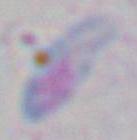

Summary:
  - Modality: photomicrograph
  - Magnification: 1000x
  - Identification: Toxoplasma gondii